Classify this cell by malaria status.
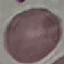

It is uninfected.

Cell patch, automatically extracted from a larger field of view and resized to 64 × 64 pixels. Thin blood film. Giemsa stain. Acquired by smartphone through the microscope eyepiece.